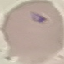

result = no malaria parasites detected
preparation = thin blood smear
stain = Giemsa
image type = cell patch, automatically extracted from a larger field of view and resized to 64 × 64 pixels
capture = smartphone camera at the microscope eyepiece